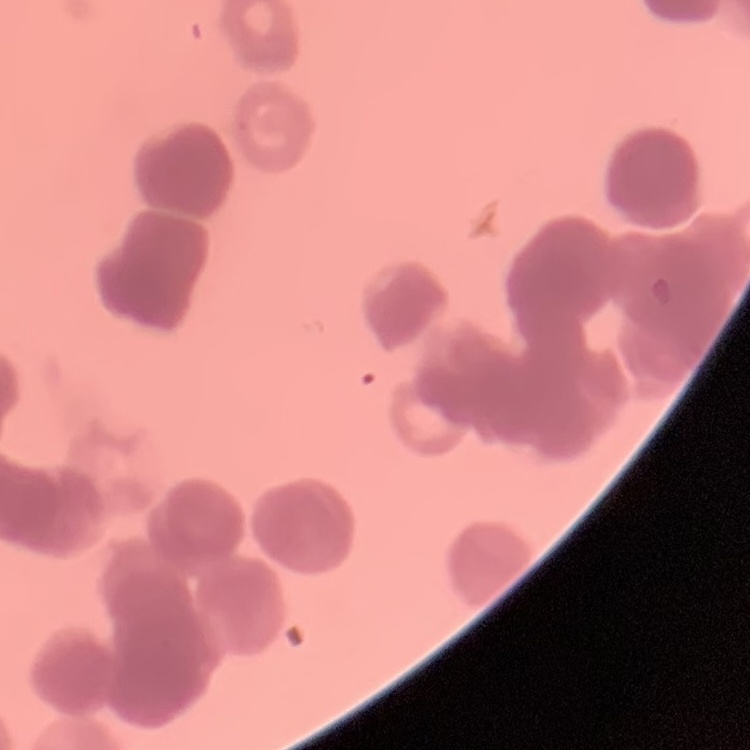
Summary:
  - Erythrocyte morphology: rouleaux formation
  - Image type: square crop of a larger photomicrograph
  - Preparation: thin peripheral smear
  - Stain: Field's or Giemsa